Locate every Plasmodium falciparum-infected red blood cell.
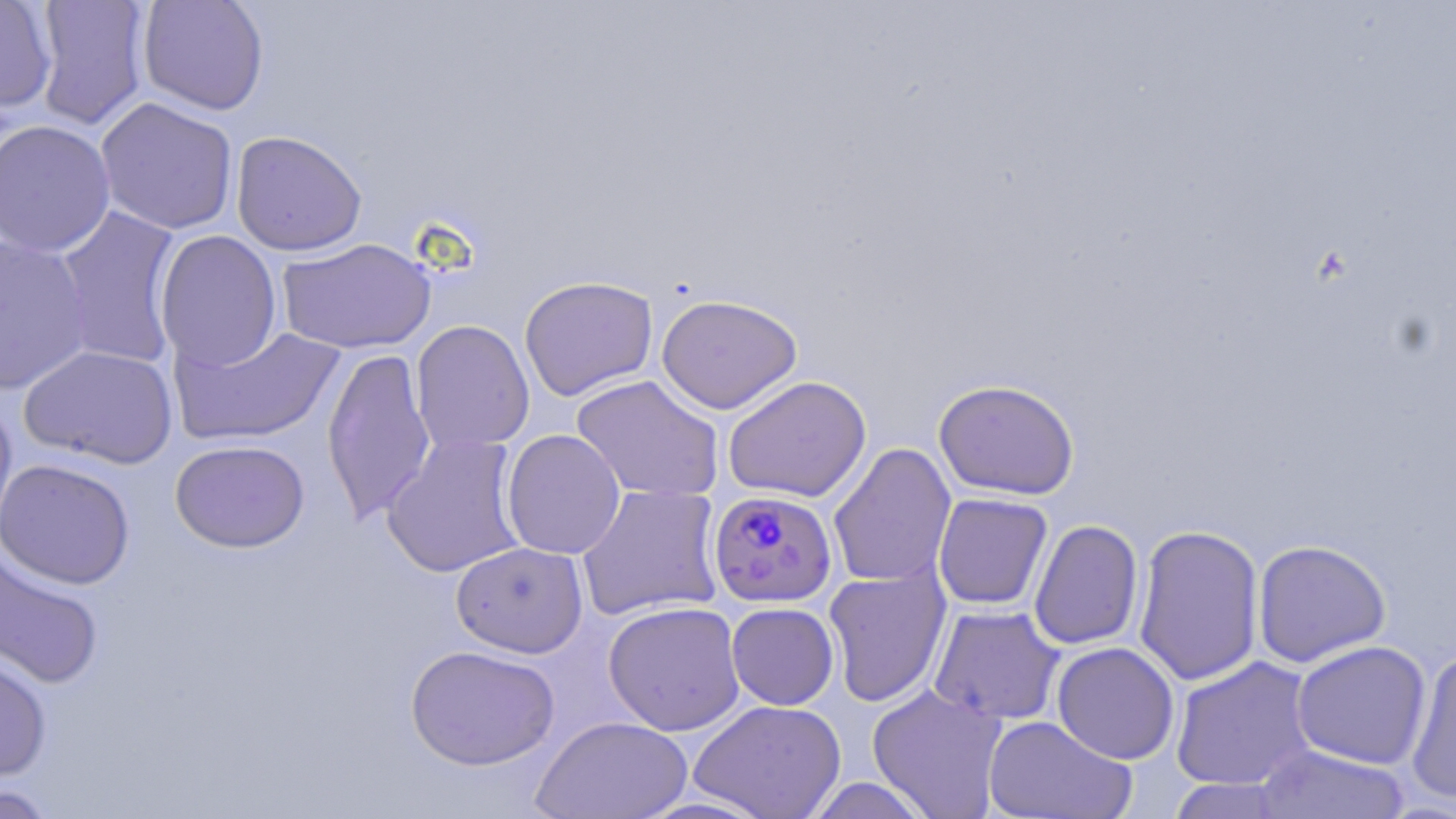

Approximate bounding boxes as [x1, y1, x2, y2] in pixels.
Plasmodium falciparum-infected red blood cells: [708, 489, 838, 607].

slide_level_diagnosis: Plasmodium falciparum
magnification: 1000x
preparation: thin blood smear
stain: May-Grünwald-Giemsa
uninfected_red_blood_cell_locations: 'approximate bounding boxes as [x1, y1, x2, y2] in pixels: [0, 0, 56, 113], [137, 0, 270, 115], [32, 1, 151, 130], [95, 97, 239, 235], [0, 119, 116, 257], [231, 130, 367, 256], [53, 205, 185, 370], [154, 231, 282, 370], [0, 235, 93, 396], [277, 237, 437, 354], [519, 275, 659, 402], [656, 293, 803, 414], [410, 320, 535, 454], [169, 322, 345, 447], [19, 344, 179, 469], [322, 346, 436, 525], [570, 375, 725, 503], [722, 375, 872, 503], [933, 378, 1080, 500], [0, 393, 17, 548], [501, 429, 626, 560], [382, 433, 526, 578], [170, 439, 310, 553], [828, 443, 957, 589], [0, 458, 135, 589], [576, 483, 724, 622], [933, 493, 1053, 610], [1029, 519, 1144, 650], [1133, 523, 1264, 686], [1252, 539, 1391, 667], [451, 541, 588, 658], [0, 547, 106, 691], [823, 566, 951, 708], [602, 601, 746, 736], [726, 602, 839, 710], [929, 605, 1066, 725], [1291, 640, 1431, 770], [1052, 642, 1180, 765], [0, 644, 53, 783], [405, 644, 560, 771], [1405, 649, 1456, 805], [1170, 656, 1318, 791], [867, 684, 1008, 819], [688, 699, 847, 819], [983, 714, 1136, 819], [532, 715, 692, 819], [1252, 744, 1412, 819], [804, 777, 934, 818], [1165, 777, 1292, 818], [0, 783, 60, 818]'
field_of_view: single
modality: light microscopy
image_size: 1456×819 pixels